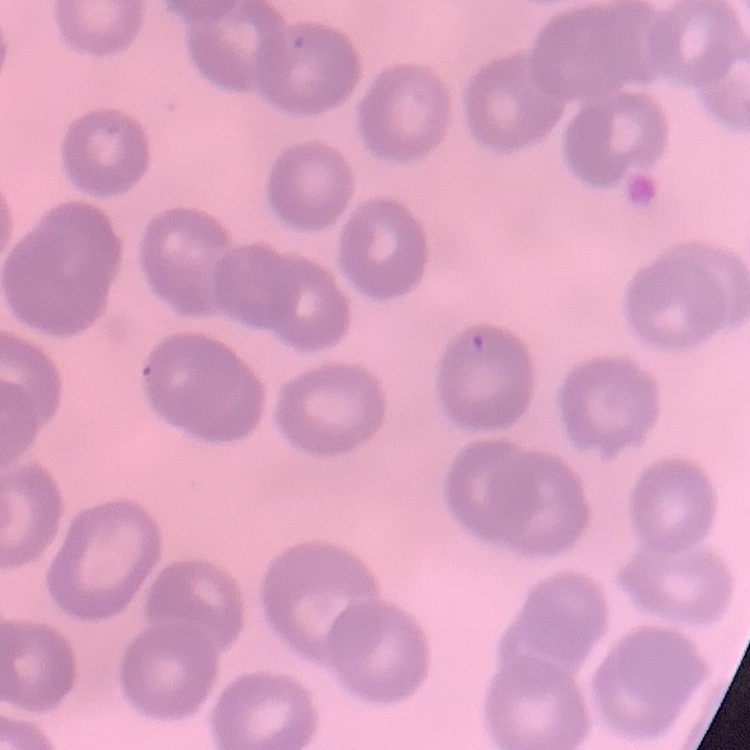

Summary:
  - Red blood cell morphology: no rouleaux formation
  - Image type: one tile cut from a larger photomicrograph
  - Stain: Field's or Giemsa
  - Preparation: thin peripheral smear